Classify this cell by malaria status.
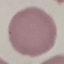

It is uninfected.

Summary:
  - Image type: cell patch, automatically extracted from a larger field of view and resized to 64 × 64 pixels
  - Capture: smartphone camera at the microscope eyepiece
  - Preparation: thin smear
  - Stain: Giemsa